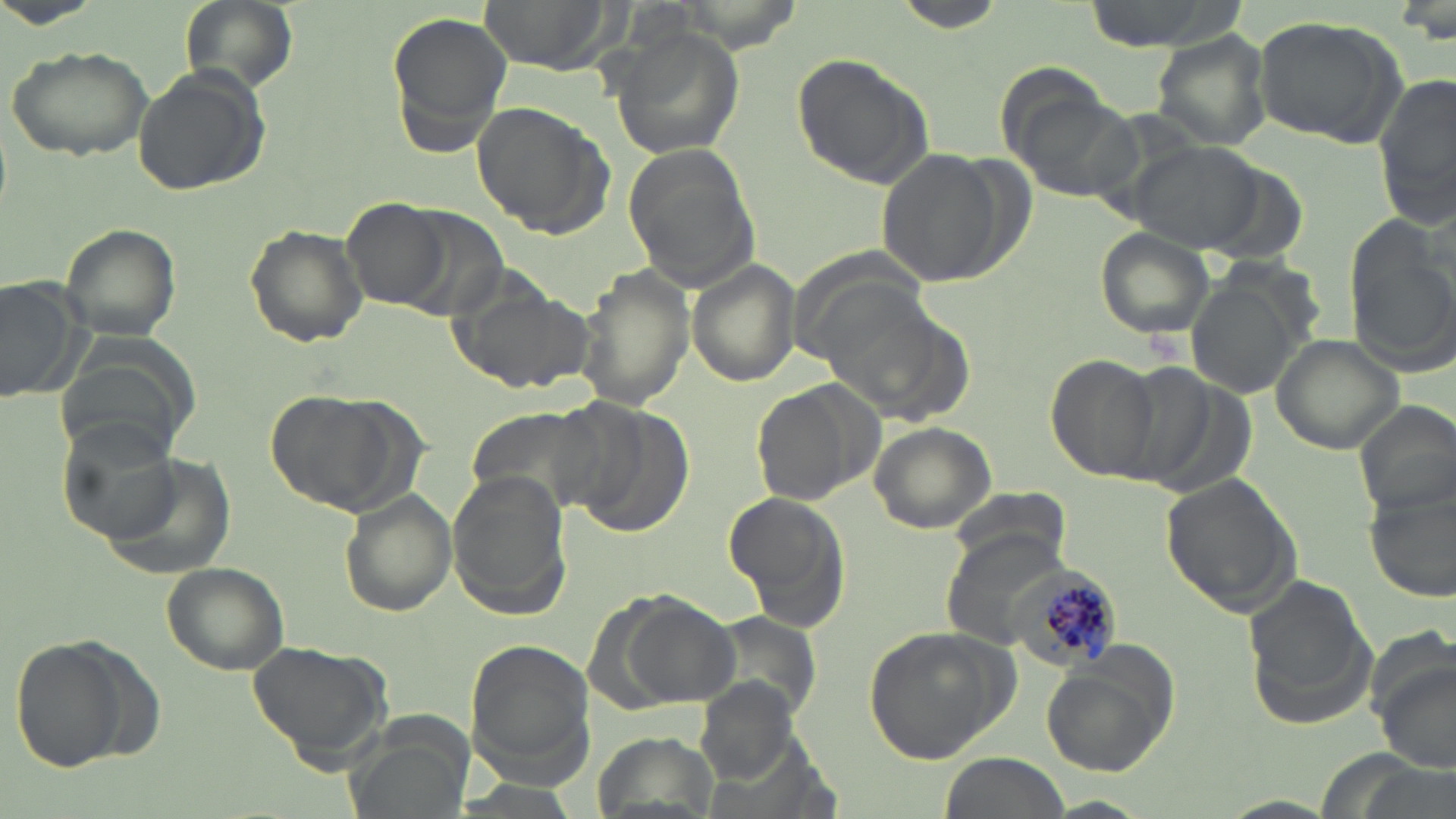
Summary:
  - Coordinate format: approximate bounding boxes as (x1,y1)-(x2,y2) corner pairs in pixels
  - Plasmodium malariae-infected red blood cell locations: (1005,562)-(1122,670)
  - Uninfected red blood cell locations: (178,0)-(299,93), (478,0)-(620,74), (892,0)-(1012,35), (1077,0)-(1242,53), (386,9)-(510,153), (1251,15)-(1407,146), (609,24)-(744,162), (1154,32)-(1274,148), (4,44)-(154,161), (791,52)-(935,187), (132,63)-(268,198), (1376,69)-(1456,226), (1012,90)-(1147,202), (471,101)-(610,234), (1130,143)-(1267,253), (623,145)-(762,294), (879,150)-(1004,286), (343,199)-(453,311), (243,223)-(370,347), (59,224)-(185,341), (1096,226)-(1217,341), (1348,226)-(1456,372), (687,259)-(802,386), (576,266)-(691,409), (448,277)-(594,397), (0,278)-(88,405), (1186,278)-(1306,399), (1271,334)-(1407,455), (1046,355)-(1161,482), (752,381)-(877,507), (267,392)-(404,513), (555,395)-(696,533), (1353,399)-(1456,515), (466,408)-(605,515), (57,418)-(187,548), (868,423)-(997,534), (446,470)-(572,620), (1159,471)-(1302,615), (1365,482)-(1454,603), (951,485)-(1070,580), (339,490)-(455,618), (721,493)-(851,623), (944,532)-(1070,638), (161,560)-(289,673), (1241,575)-(1378,728), (610,594)-(739,707), (863,624)-(1013,763), (10,637)-(130,772), (466,638)-(598,784), (244,640)-(394,770), (1373,654)-(1455,775), (1039,655)-(1176,778), (938,753)-(1068,819), (1044,797)-(1153,817), (1221,797)-(1339,818)
  - Slide-level diagnosis: Plasmodium malariae
  - Preparation: thin blood film
  - Image size: 1456×819 pixels
  - Stain: May-Grünwald-Giemsa
  - Modality: light microscopy
  - Field of view: single
  - Magnification: 1000x